Describe the morphology of the red blood cells.
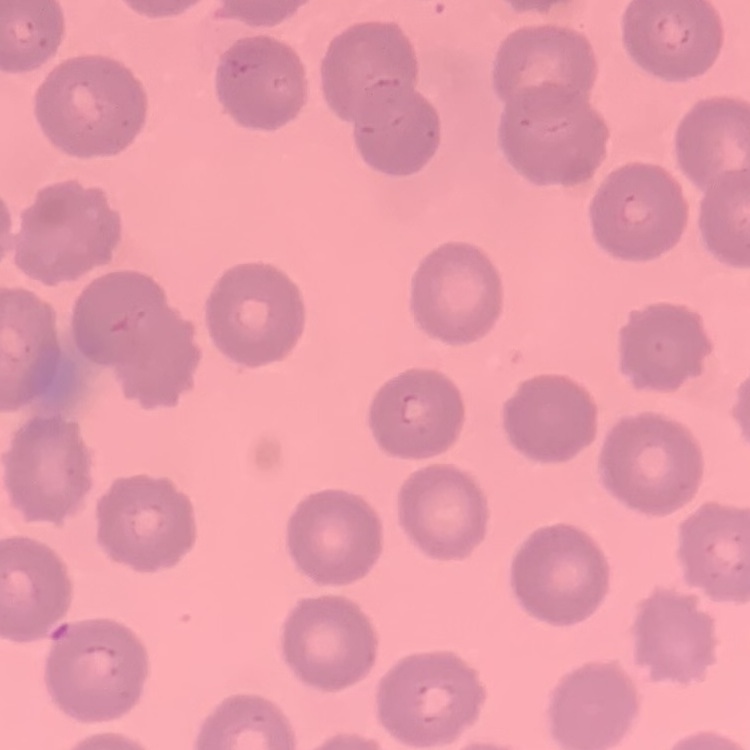
They show no rouleaux formation.

One tile cut from a larger photomicrograph. Thin blood film. Stained with either Field's or Giemsa.